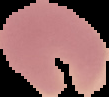
image size = 109×97 pixels
image type = segmented cell region with the area outside set to black
malaria status = uninfected
preparation = thin blood smear